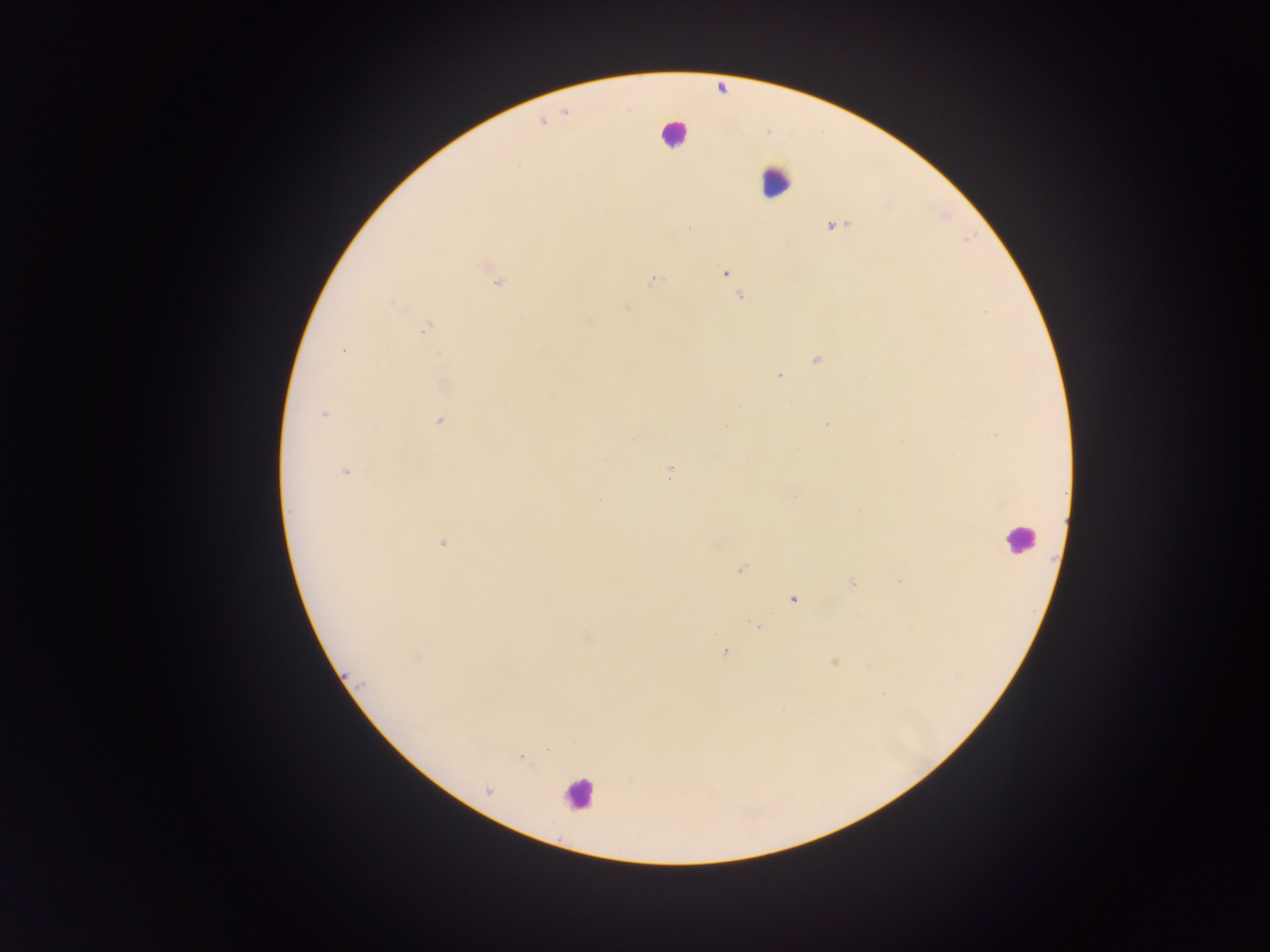
{
  "capture": "mobile-phone photograph through a microscope",
  "leukocyte_locations": "approximate centers as [x, y] in pixels: [673, 133], [775, 181], [1018, 538], [578, 793]",
  "field_of_view": "single",
  "image_size": "1270×952 pixels",
  "country": "Ghana",
  "preparation": "thick blood film",
  "plasmodium_parasite_locations": "approximate centers as [x, y] in pixels: [835, 226], [688, 229], [725, 273], [653, 279], [497, 282], [740, 297], [395, 304], [627, 308], [589, 320], [426, 329], [343, 350], [817, 360], [779, 375], [324, 414], [439, 421], [827, 424], [633, 438], [901, 442], [669, 470], [345, 472], [442, 543], [740, 570], [899, 581], [852, 583], [793, 599], [757, 626], [588, 637], [724, 652], [417, 657], [835, 663], [957, 675], [521, 758], [487, 791]"
}